Classify this cell by malaria status.
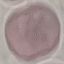
It is uninfected.

Summary:
  - Capture: smartphone through the microscope eyepiece
  - Image type: cell patch, automatically extracted from a larger field of view and resized to 64 × 64 pixels
  - Preparation: thin smear
  - Stain: Giemsa